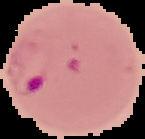 Malaria status: parasitized. The area outside the segmented cell region is set to black. From a thin blood smear. Image is 145×139 pixels.